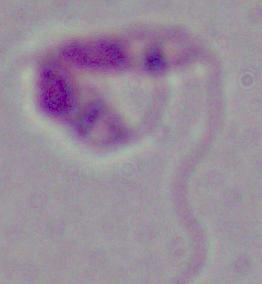
{
  "modality": "micrograph",
  "magnification": "1000x",
  "identification": "Leishmania"
}